Outline each Plasmodium falciparum-infected red blood cell.
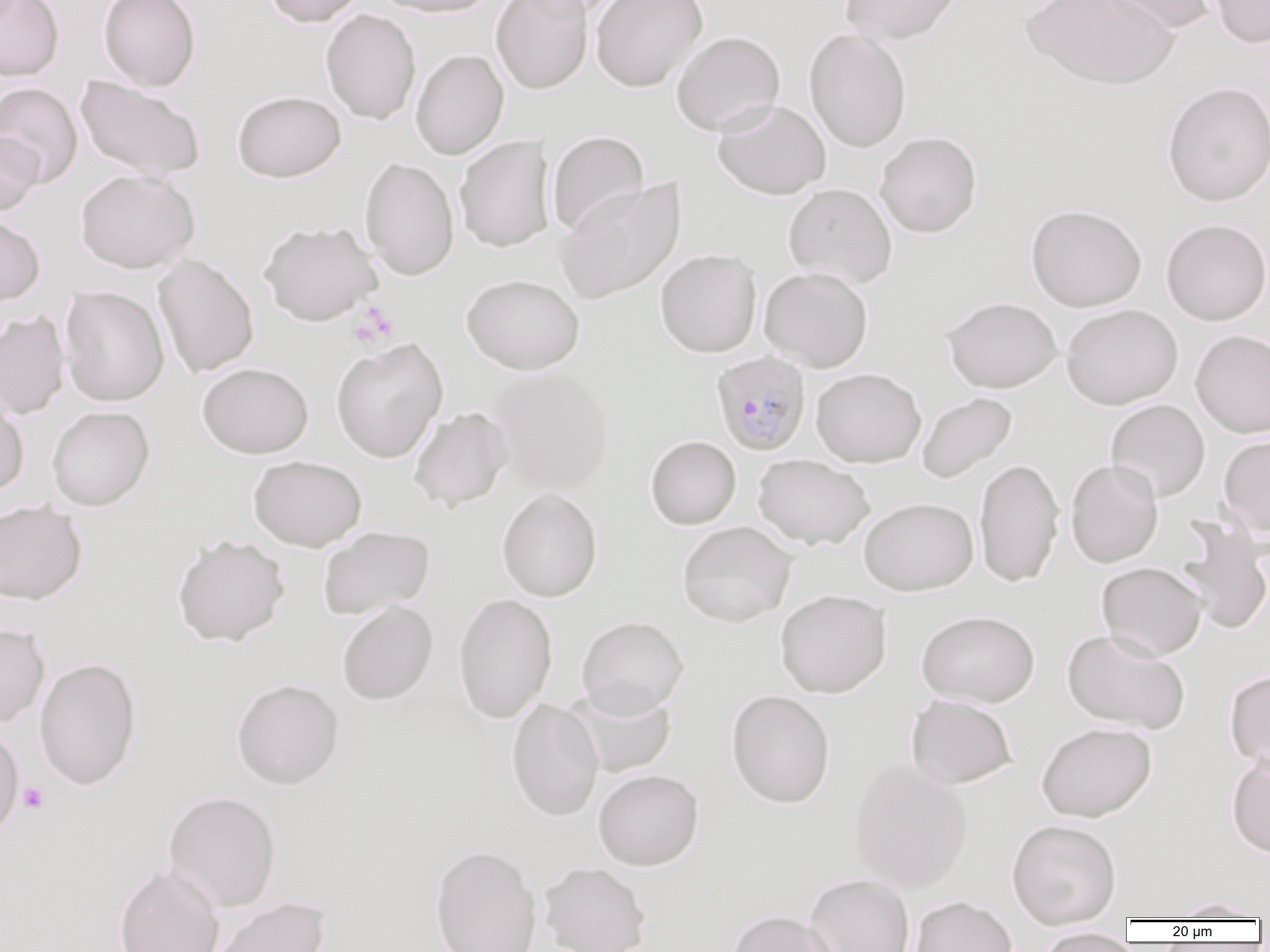

Approximate bounding boxes as named x1/y1/x2/y2 corners in pixels.
Plasmodium falciparum-infected red blood cells: (x1=711, y1=350, x2=812, y2=456).

Uninfected red blood cell locations: (x1=0, y1=0, x2=64, y2=81), (x1=98, y1=0, x2=201, y2=91), (x1=262, y1=0, x2=365, y2=28), (x1=371, y1=0, x2=501, y2=18), (x1=491, y1=0, x2=593, y2=94), (x1=511, y1=0, x2=629, y2=22), (x1=590, y1=0, x2=707, y2=92), (x1=839, y1=0, x2=962, y2=45), (x1=1020, y1=0, x2=1180, y2=90), (x1=1098, y1=0, x2=1218, y2=36), (x1=1209, y1=0, x2=1270, y2=48), (x1=321, y1=9, x2=421, y2=125), (x1=803, y1=28, x2=912, y2=153), (x1=670, y1=30, x2=785, y2=137), (x1=410, y1=48, x2=508, y2=160), (x1=75, y1=75, x2=206, y2=181), (x1=1161, y1=81, x2=1270, y2=207), (x1=0, y1=82, x2=84, y2=187), (x1=232, y1=90, x2=346, y2=183), (x1=712, y1=99, x2=831, y2=200), (x1=547, y1=130, x2=649, y2=237), (x1=0, y1=131, x2=43, y2=216), (x1=874, y1=131, x2=983, y2=238), (x1=454, y1=135, x2=556, y2=253), (x1=359, y1=157, x2=460, y2=281), (x1=75, y1=169, x2=200, y2=273), (x1=554, y1=178, x2=685, y2=304), (x1=782, y1=183, x2=897, y2=289), (x1=1025, y1=203, x2=1147, y2=312), (x1=0, y1=213, x2=45, y2=307), (x1=1160, y1=218, x2=1270, y2=326), (x1=258, y1=219, x2=383, y2=326), (x1=655, y1=241, x2=762, y2=350), (x1=152, y1=253, x2=260, y2=378), (x1=759, y1=266, x2=873, y2=372), (x1=461, y1=273, x2=585, y2=374), (x1=59, y1=286, x2=169, y2=407), (x1=941, y1=295, x2=1063, y2=393), (x1=1061, y1=304, x2=1183, y2=410), (x1=0, y1=310, x2=70, y2=419), (x1=1190, y1=329, x2=1270, y2=439), (x1=330, y1=337, x2=448, y2=463), (x1=197, y1=362, x2=314, y2=458), (x1=811, y1=367, x2=926, y2=468), (x1=490, y1=368, x2=614, y2=494), (x1=0, y1=389, x2=30, y2=497), (x1=916, y1=392, x2=1017, y2=484), (x1=1105, y1=399, x2=1210, y2=503), (x1=46, y1=406, x2=155, y2=511), (x1=408, y1=406, x2=512, y2=511), (x1=1218, y1=434, x2=1270, y2=535), (x1=645, y1=436, x2=741, y2=529), (x1=753, y1=454, x2=874, y2=549), (x1=248, y1=455, x2=367, y2=552), (x1=973, y1=457, x2=1065, y2=588), (x1=1065, y1=459, x2=1164, y2=568), (x1=497, y1=487, x2=602, y2=602), (x1=858, y1=497, x2=978, y2=595), (x1=0, y1=500, x2=87, y2=605), (x1=1174, y1=516, x2=1270, y2=635), (x1=677, y1=521, x2=797, y2=627), (x1=318, y1=526, x2=435, y2=620), (x1=171, y1=533, x2=291, y2=647), (x1=1096, y1=561, x2=1208, y2=661), (x1=774, y1=589, x2=892, y2=698), (x1=453, y1=593, x2=558, y2=724), (x1=336, y1=600, x2=439, y2=706), (x1=916, y1=609, x2=1040, y2=707), (x1=576, y1=615, x2=689, y2=717), (x1=0, y1=623, x2=50, y2=727), (x1=1062, y1=627, x2=1190, y2=735), (x1=34, y1=657, x2=143, y2=791), (x1=1224, y1=669, x2=1270, y2=773), (x1=230, y1=677, x2=345, y2=790), (x1=564, y1=684, x2=679, y2=779), (x1=725, y1=689, x2=835, y2=808), (x1=905, y1=694, x2=1018, y2=789), (x1=506, y1=698, x2=604, y2=822), (x1=1035, y1=721, x2=1157, y2=822), (x1=0, y1=725, x2=25, y2=843), (x1=1226, y1=755, x2=1270, y2=858), (x1=848, y1=757, x2=974, y2=893), (x1=592, y1=768, x2=704, y2=870), (x1=161, y1=790, x2=283, y2=913), (x1=1006, y1=818, x2=1122, y2=929), (x1=428, y1=844, x2=543, y2=952), (x1=539, y1=861, x2=652, y2=952), (x1=113, y1=863, x2=225, y2=952), (x1=804, y1=873, x2=915, y2=952), (x1=910, y1=895, x2=1018, y2=952), (x1=204, y1=896, x2=332, y2=952), (x1=1163, y1=897, x2=1267, y2=921), (x1=726, y1=909, x2=839, y2=952), (x1=1036, y1=927, x2=1134, y2=952). Platelet locations: (x1=352, y1=302, x2=398, y2=348), (x1=18, y1=783, x2=48, y2=813). Slide-level diagnosis: Plasmodium falciparum. Light microscopy. One field of a larger specimen. Image is 1270×952 pixels. Thin blood film. 1000x magnification.